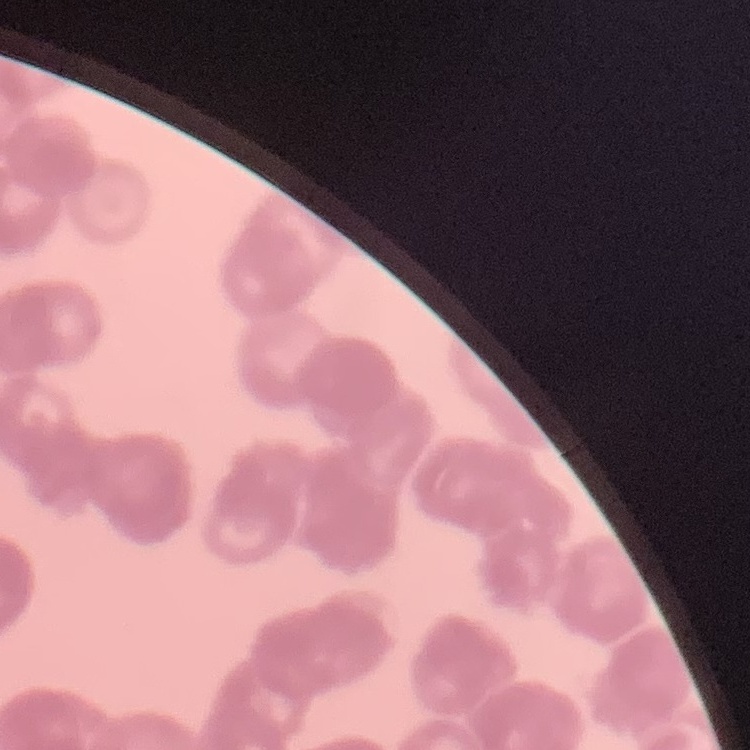

{
  "red_blood_cell_morphology": "rouleaux formation",
  "preparation": "thin peripheral smear",
  "stain": "Field's or Giemsa",
  "image_type": "square crop of a larger photomicrograph"
}